Locate and identify every blood parasite.
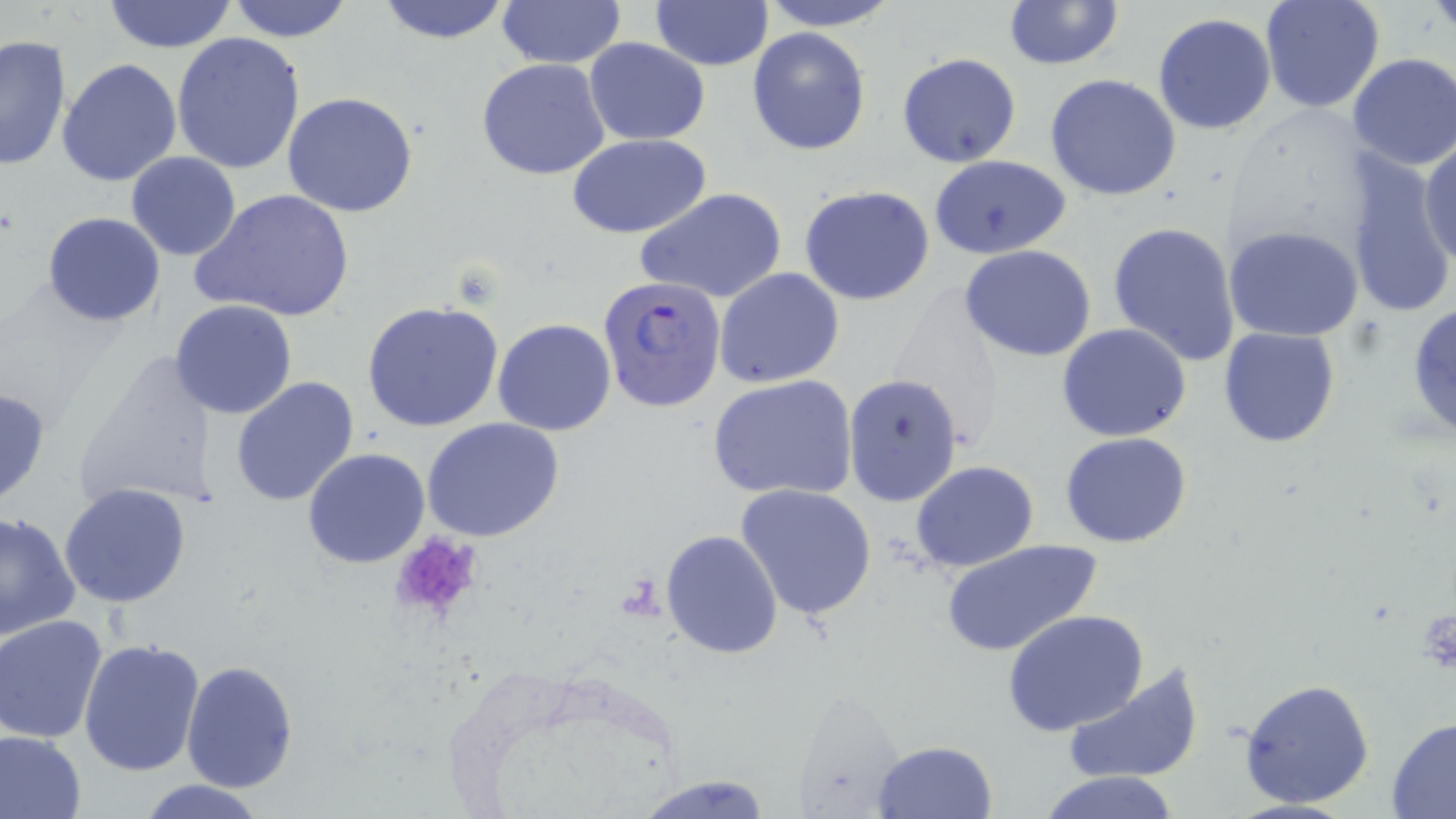
Approximate bounding boxes as (x1,y1)-(x2,y2) corner pairs in pixels.
Plasmodium falciparum-infected red blood cells: (598,276)-(726,414).
No Plasmodium ovale, Plasmodium malariae, Plasmodium vivax, Babesia divergens, or Trypanosoma brucei observed.

Summary:
  - Platelet locations: (387,534)-(484,625)
  - Uninfected red blood cell locations: (100,0)-(239,53), (227,0)-(354,43), (496,0)-(624,68), (650,0)-(774,69), (757,0)-(901,31), (1002,0)-(1124,71), (1258,0)-(1385,115), (374,1)-(515,46), (1152,13)-(1276,135), (748,28)-(872,156), (173,32)-(306,175), (0,34)-(71,171), (584,38)-(710,145), (896,53)-(1021,168), (1346,54)-(1456,171), (476,57)-(611,180), (58,58)-(183,187), (1045,73)-(1183,202), (282,91)-(418,217), (568,134)-(712,238), (1419,137)-(1455,268), (1343,150)-(1453,321), (126,151)-(242,261), (928,154)-(1072,259), (799,186)-(936,305), (635,187)-(788,305), (193,188)-(356,325), (42,212)-(166,326), (1107,221)-(1241,367), (1225,225)-(1364,343), (960,246)-(1098,363), (715,267)-(843,387), (1406,299)-(1456,443), (172,301)-(298,420), (363,302)-(505,433), (493,319)-(617,437), (1057,324)-(1193,442), (1217,327)-(1341,447), (75,350)-(221,514), (842,373)-(964,507), (230,375)-(361,507), (707,376)-(859,500), (420,417)-(565,542), (1061,432)-(1193,548), (302,447)-(431,569), (910,461)-(1039,571), (733,482)-(879,622), (60,483)-(190,608), (0,508)-(82,642), (660,529)-(784,661), (941,537)-(1104,658), (1004,608)-(1149,738), (1,614)-(108,744), (77,638)-(205,778), (182,660)-(299,794), (1062,663)-(1205,785), (1238,677)-(1376,811), (789,703)-(925,819), (1386,717)-(1456,816), (0,730)-(86,818), (873,740)-(998,818), (1038,770)-(1181,819), (634,774)-(772,818), (135,779)-(271,817)
  - Slide-level diagnosis: Plasmodium falciparum
  - Field of view: one of a larger specimen
  - Stain: May-Grünwald-Giemsa
  - Image size: 1456×819 pixels
  - Preparation: thin blood film
  - Modality: optical microscopy
  - Magnification: 1000x